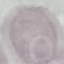
Summary:
  - Malaria status: uninfected
  - Image type: automatically extracted cell patch, resized to 64 × 64 pixels
  - Preparation: thin smear
  - Capture: smartphone camera at the microscope eyepiece
  - Stain: Giemsa